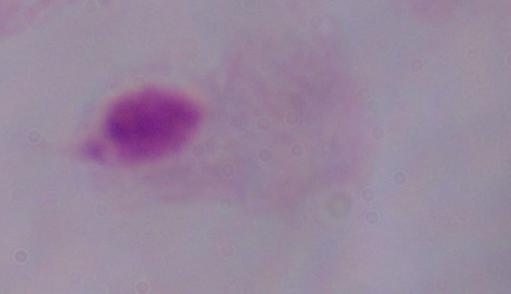

Summary:
  - Magnification: 1000x
  - Identification: trichomonad
  - Modality: photomicrograph